Identify the parasite.
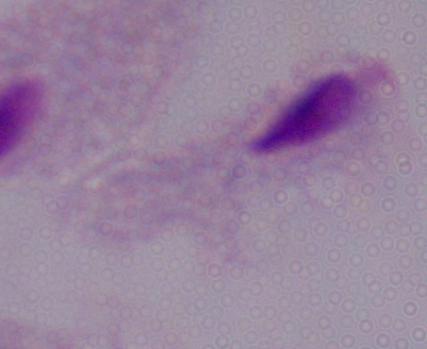

A trichomonad.

Summary:
  - Magnification: 1000x
  - Modality: photomicrograph